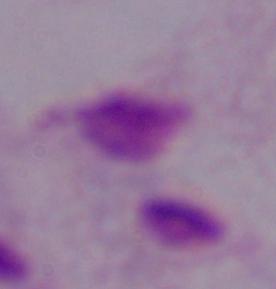

identification = trichomonad
magnification = 1000x
modality = photomicrograph